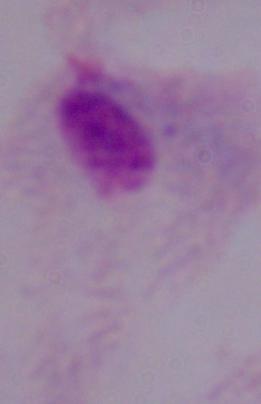 Micrograph. 1000x magnification. A trichomonad is seen.